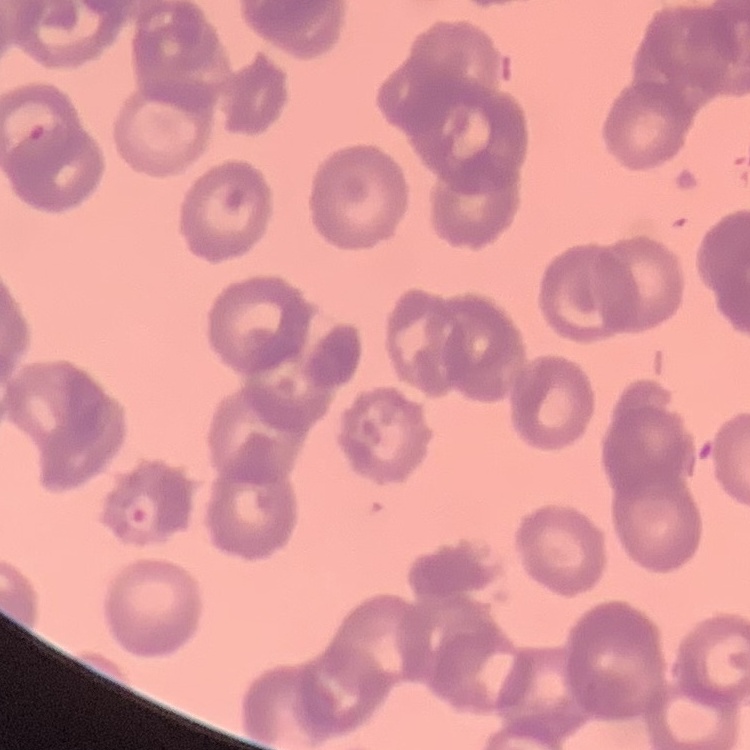

{
  "red_blood_cell_morphology": "rouleaux formation",
  "stain": "Field's or Giemsa",
  "preparation": "thin peripheral smear",
  "image_type": "square crop of a larger photomicrograph"
}